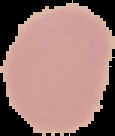

Summary:
  - Image size: 115×136 pixels
  - Result: negative for malaria parasites
  - Image type: cell region segmented out of the field of view; surrounding area masked to black
  - Preparation: thin blood smear